Find the red blood cells that are infected with P. falciparum, and any of indeterminate infection status.
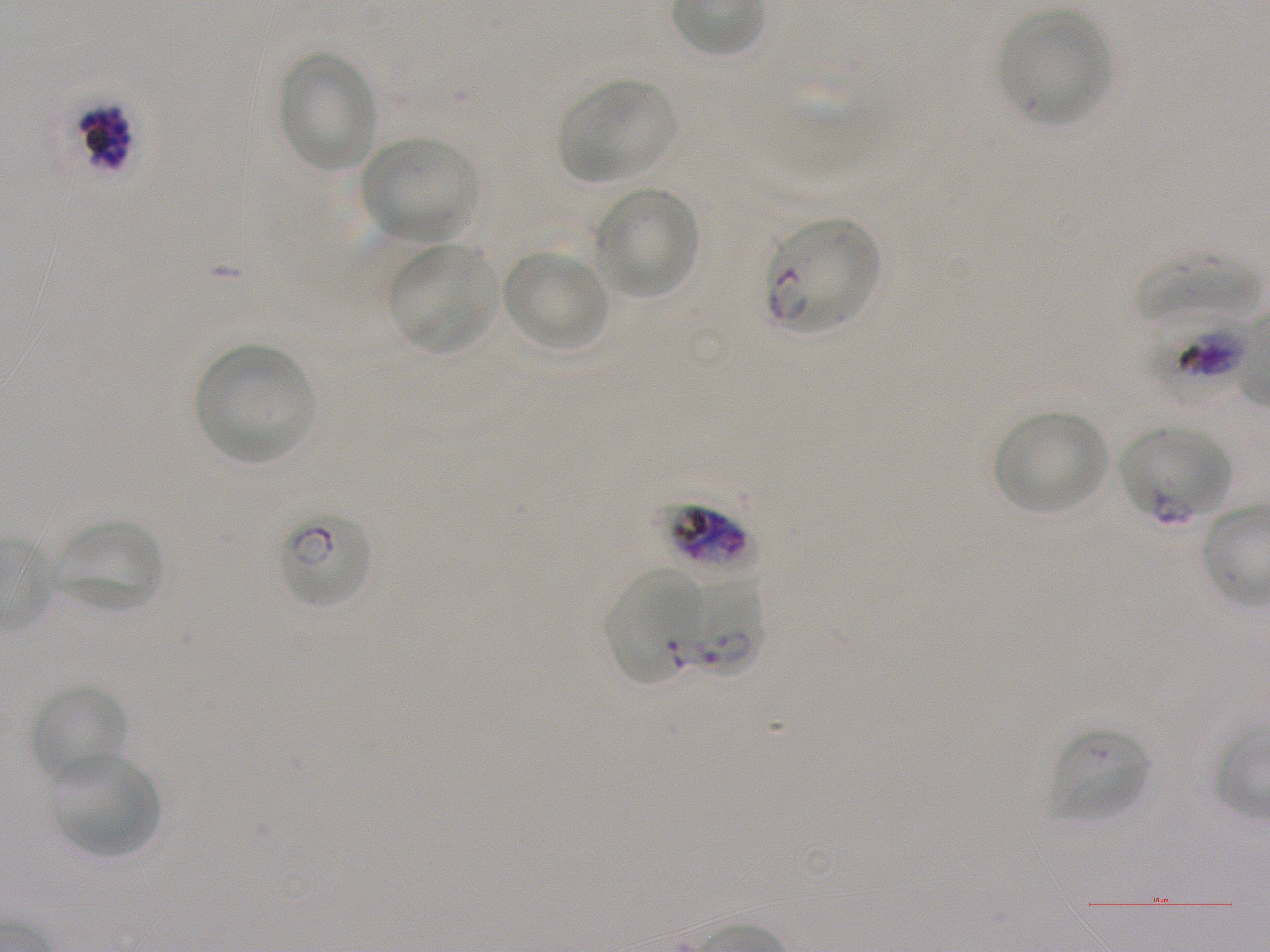
Approximate bounding boxes as {x1, y1, x2, y2} in pixels. Not every red blood cell is marked. A life-cycle stage — or a range of stages, where the recorded stages span more than one — follows each staged infected red blood cell.
Infected red blood cells: {51, 94, 133, 175}; {764, 218, 881, 333} late ring; {1141, 308, 1254, 401} early trophozoite to early schizont; {1119, 425, 1231, 522}; {279, 514, 372, 610} early ring to early trophozoite; {600, 571, 700, 687}; {681, 574, 767, 680} ring.
Red blood cells of indeterminate infection status: {660, 500, 752, 574}.

Summary:
  - Locations of uninfected red blood cells: {998, 11, 1112, 125}, {278, 51, 380, 173}, {558, 78, 676, 183}, {360, 136, 480, 241}, {592, 185, 700, 298}, {388, 242, 499, 354}, {502, 250, 608, 353}, {1134, 255, 1262, 322}, {195, 343, 314, 465}, {994, 411, 1110, 516}, {54, 519, 163, 613}, {30, 683, 129, 787}, {1050, 726, 1150, 823}, {50, 753, 161, 859}
  - Donor blood group: A+
  - Stain: Giemsa
  - Objective: 100x, oil immersion, numerical aperture 1.25
  - Culture: P. falciparum strain NF54, static, in vitro
  - Preparation: thin blood film
  - Image size: 1270×952 pixels
  - Field of view: one from this slide